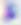

400x magnification. Photomicrograph. Toxoplasma gondii is seen.